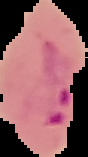
Summary:
  - Image type: segmented cell region on a black background
  - Preparation: thin blood smear
  - Image size: 88×157 pixels
  - Malaria status: parasitized